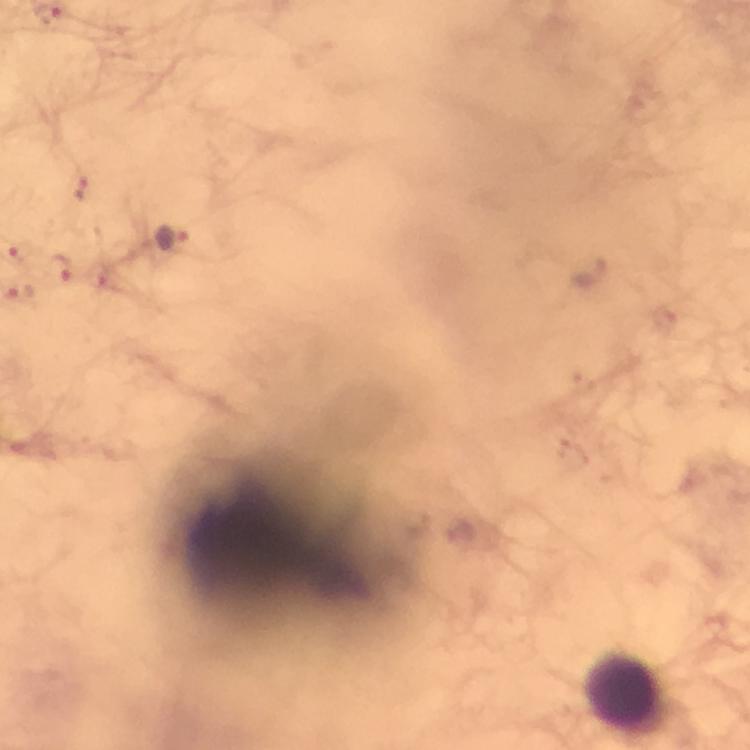

stain: Giemsa
capture: smartphone camera through the microscope
plasmodium_parasite_locations: 'approximate centers as (x, y) in pixels: (81, 189), (172, 239), (61, 270), (20, 293)'
magnification: 100x
leukocyte_locations: 'approximate centers as (x, y) in pixels: (627, 691)'
cropped_from: one field of view
preparation: thick blood film
immersion_oil: used
image_size: 750×750 pixels
context: from a diagnostic examination for malaria